Comment on the morphology of the erythrocytes.
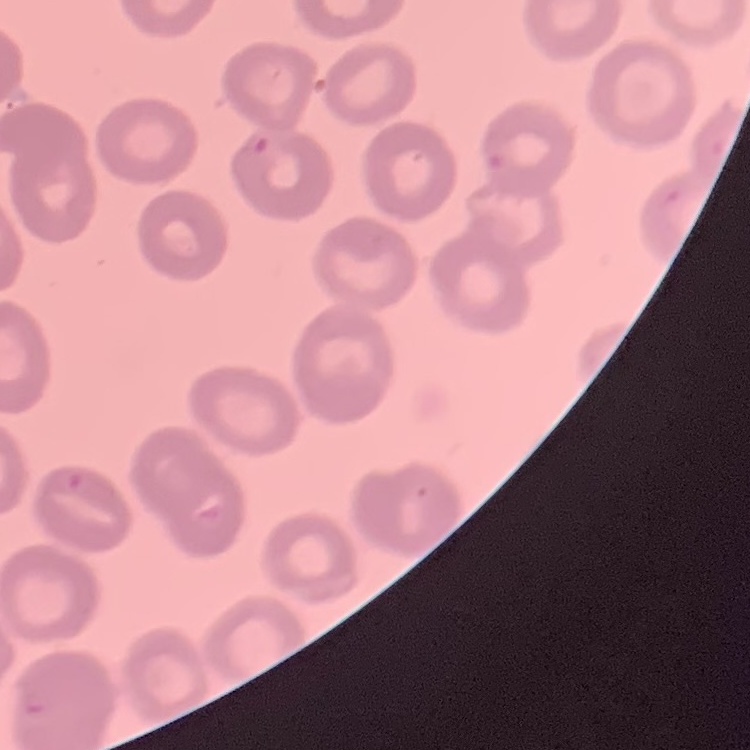

No rouleaux formation.

Thin blood smear. Square crop of a larger photomicrograph. Stained with either Field's or Giemsa.